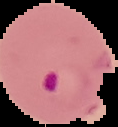
{
  "image_type": "segmented cell region on a black background",
  "result": "malaria parasites identified",
  "preparation": "thin blood film",
  "image_size": "118×127 pixels"
}